Point out each leukocyte.
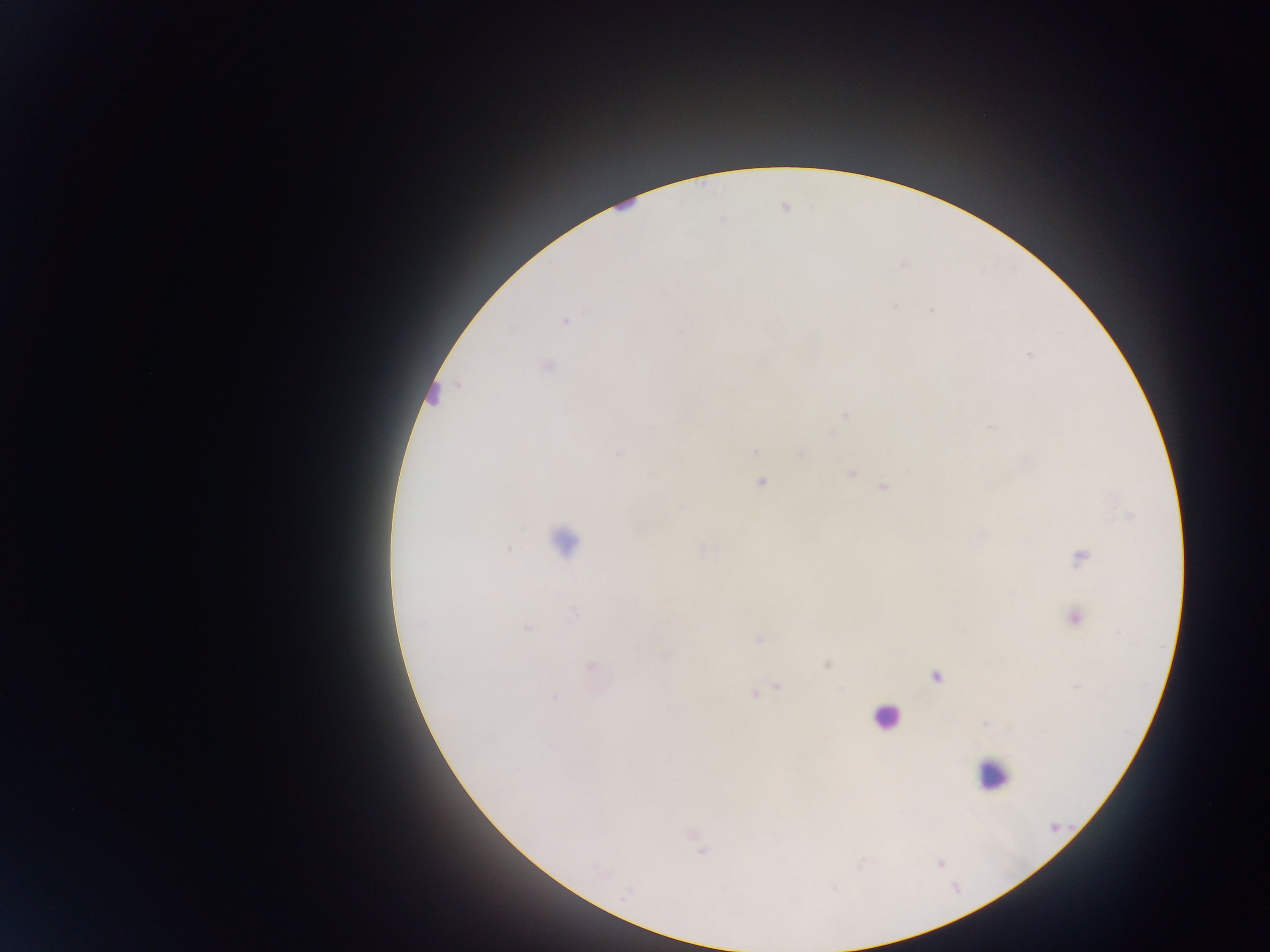

Approximate centers as {x, y} in pixels.
Leukocytes: {621, 202}, {430, 393}, {564, 540}, {885, 717}, {993, 775}.

Plasmodium parasite locations: {895, 306}, {931, 310}, {565, 322}, {1029, 355}, {548, 367}, {845, 415}, {991, 427}, {754, 452}, {618, 453}, {801, 454}, {852, 474}, {760, 483}, {884, 487}, {508, 548}, {1081, 557}, {575, 613}, {1075, 619}, {526, 628}, {759, 639}, {667, 657}, {590, 666}, {936, 677}, {778, 686}, {842, 690}, {755, 693}, {554, 697}, {985, 724}, {551, 747}, {700, 847}, {940, 863}, {599, 870}, {625, 895}. Image is 1270×952 pixels. One field of view. Photographed through a microscope with a mobile-phone camera. Thick blood smear. Sample from Ghana.